Assess this cell for malaria.
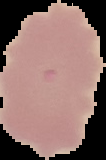

It is uninfected.

preparation = thin blood smear
image size = 106×160 pixels
image type = cell region segmented out of the field of view; surrounding area masked to black